Give the extent of all uninfected red blood cells.
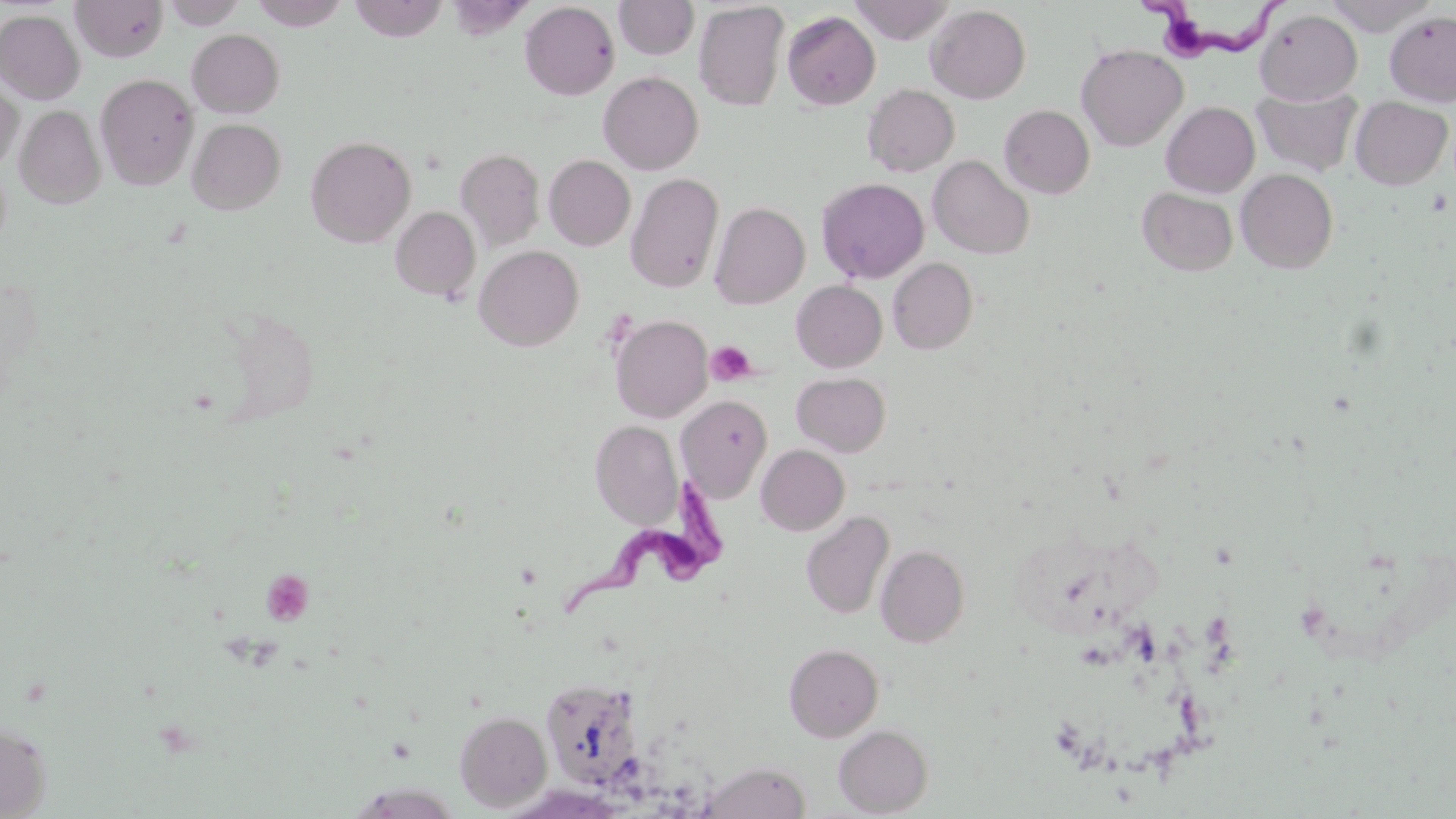

Approximate bounding boxes as (x1, y1, x2, y2) in pixels.
Uninfected red blood cells: (71, 0, 167, 62), (162, 0, 246, 29), (249, 0, 350, 30), (349, 0, 449, 42), (614, 0, 700, 60), (849, 0, 952, 44), (1322, 0, 1439, 35), (519, 2, 620, 100), (694, 2, 789, 111), (925, 5, 1031, 104), (1255, 9, 1362, 104), (0, 10, 85, 104), (782, 11, 880, 110), (1385, 11, 1456, 106), (187, 29, 285, 118), (1076, 44, 1187, 151), (598, 71, 704, 175), (95, 73, 199, 190), (0, 79, 23, 172), (863, 84, 959, 177), (1251, 86, 1362, 178), (1350, 97, 1452, 190), (1161, 101, 1259, 197), (999, 104, 1095, 198), (15, 105, 105, 209), (187, 118, 286, 214), (305, 135, 417, 248), (455, 147, 545, 250), (544, 155, 636, 251), (929, 155, 1034, 259), (1236, 169, 1338, 273), (626, 172, 724, 294), (816, 178, 929, 283), (1137, 187, 1238, 276), (709, 201, 810, 310), (390, 206, 481, 303), (474, 245, 584, 351), (888, 258, 978, 354), (792, 280, 887, 372), (610, 314, 712, 422), (792, 372, 891, 456), (676, 395, 772, 502), (590, 420, 682, 528), (757, 445, 849, 535), (801, 511, 894, 620), (876, 545, 969, 647), (784, 643, 884, 742), (540, 676, 646, 791), (454, 710, 552, 812), (0, 720, 52, 818), (834, 725, 933, 816), (702, 760, 811, 819).

Summary:
  - Platelet locations: (706, 341, 756, 386), (261, 569, 314, 626)
  - Trypanosoma brucei locations: (1141, 0, 1290, 60), (564, 478, 729, 620)
  - Slide-level diagnosis: Trypanosoma brucei
  - Magnification: 1000x
  - Field of view: single
  - Image size: 1456×819 pixels
  - Stain: May-Grünwald-Giemsa
  - Preparation: thin blood film
  - Modality: optical microscopy